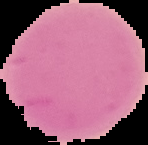
image type = segmented cell region with the area outside set to black
result = no Plasmodium parasites detected
image size = 148×145 pixels
preparation = thin blood smear